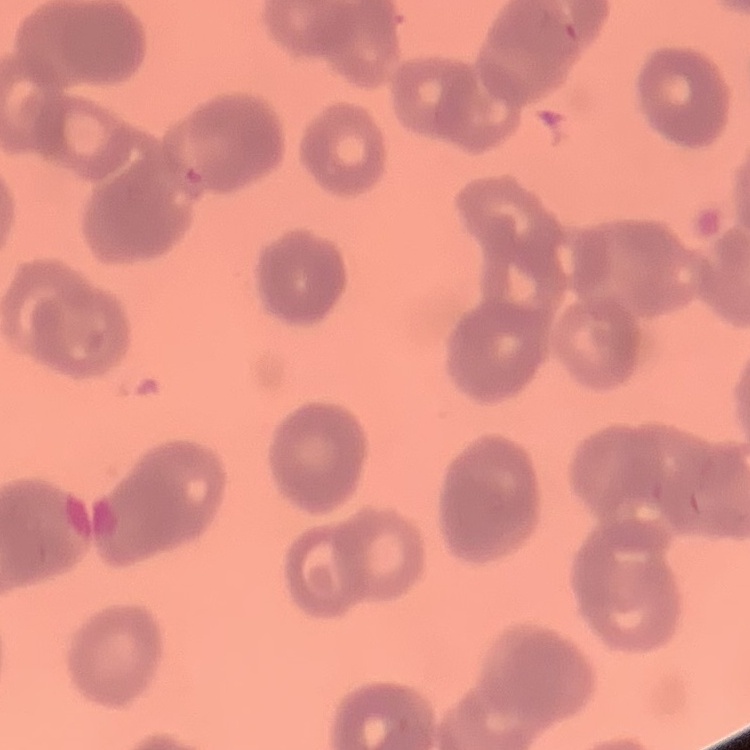
Summary:
  - Red blood cell morphology: rouleaux formation
  - Image type: square crop of a larger photomicrograph
  - Stain: Field's or Giemsa
  - Preparation: thin peripheral smear